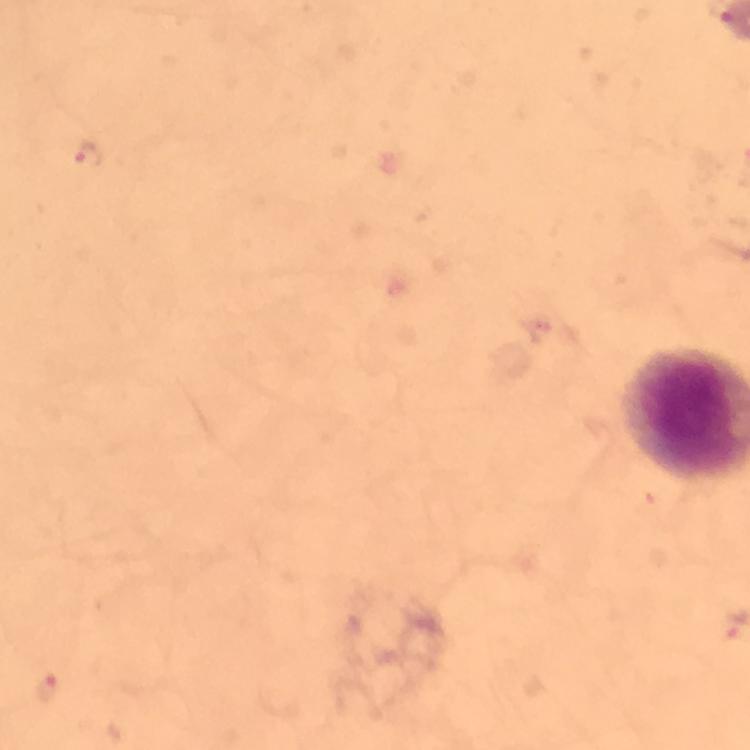
immersion oil = applied
image size = 750×750 pixels
stain = Giemsa
preparation = thick blood smear
capture = smartphone photograph through a microscope
context = from a diagnostic examination for malaria
Plasmodium parasite locations = approximate centers as (x, y) in pixels: (89, 156), (46, 687)
cropped from = one field of view
magnification = 100x